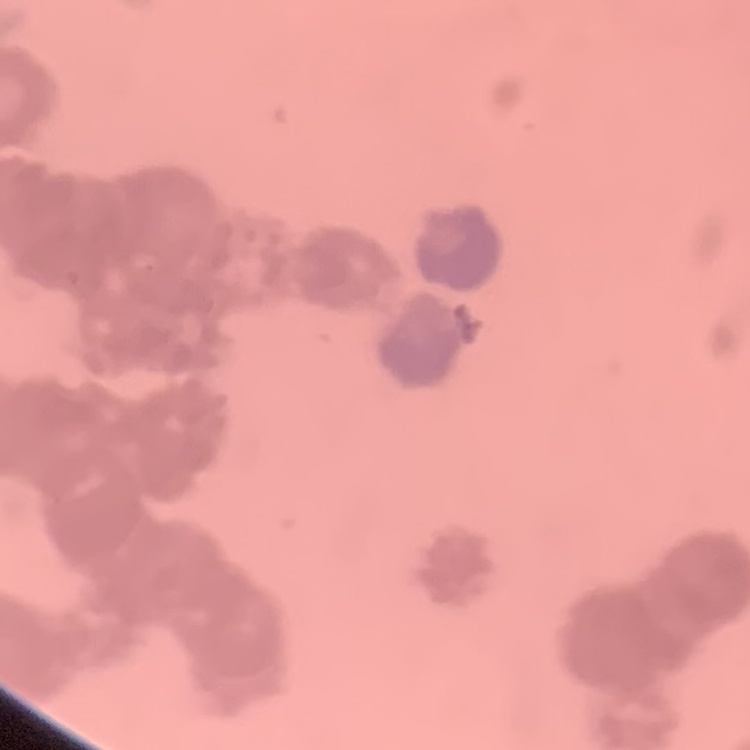
erythrocyte morphology = rouleaux formation
image type = square crop of a larger photomicrograph
preparation = thin peripheral smear
stain = Field's or Giemsa